Assess the morphology of the red blood cells.
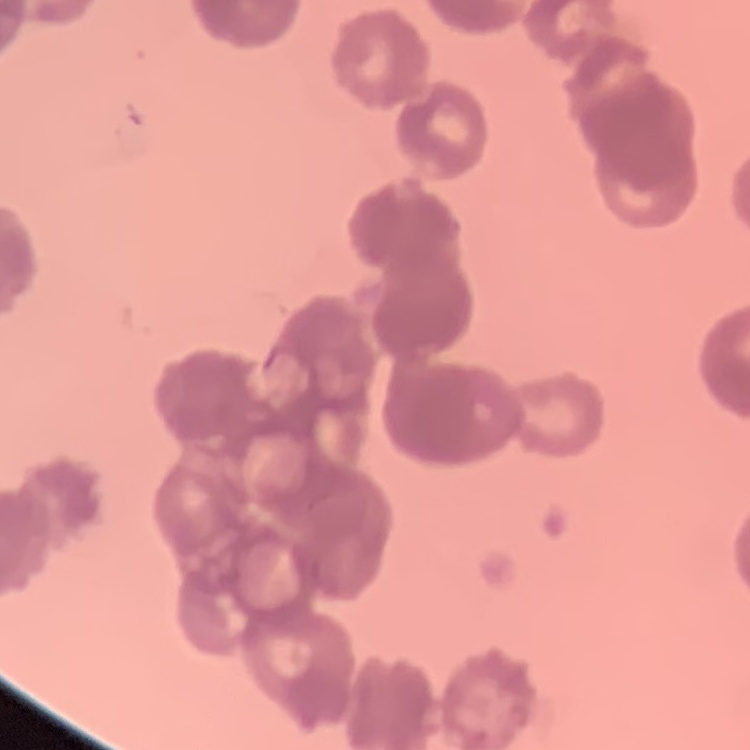

They show rouleaux formation.

Square crop of a larger photomicrograph. Thin blood film. Stained with either Field's or Giemsa.